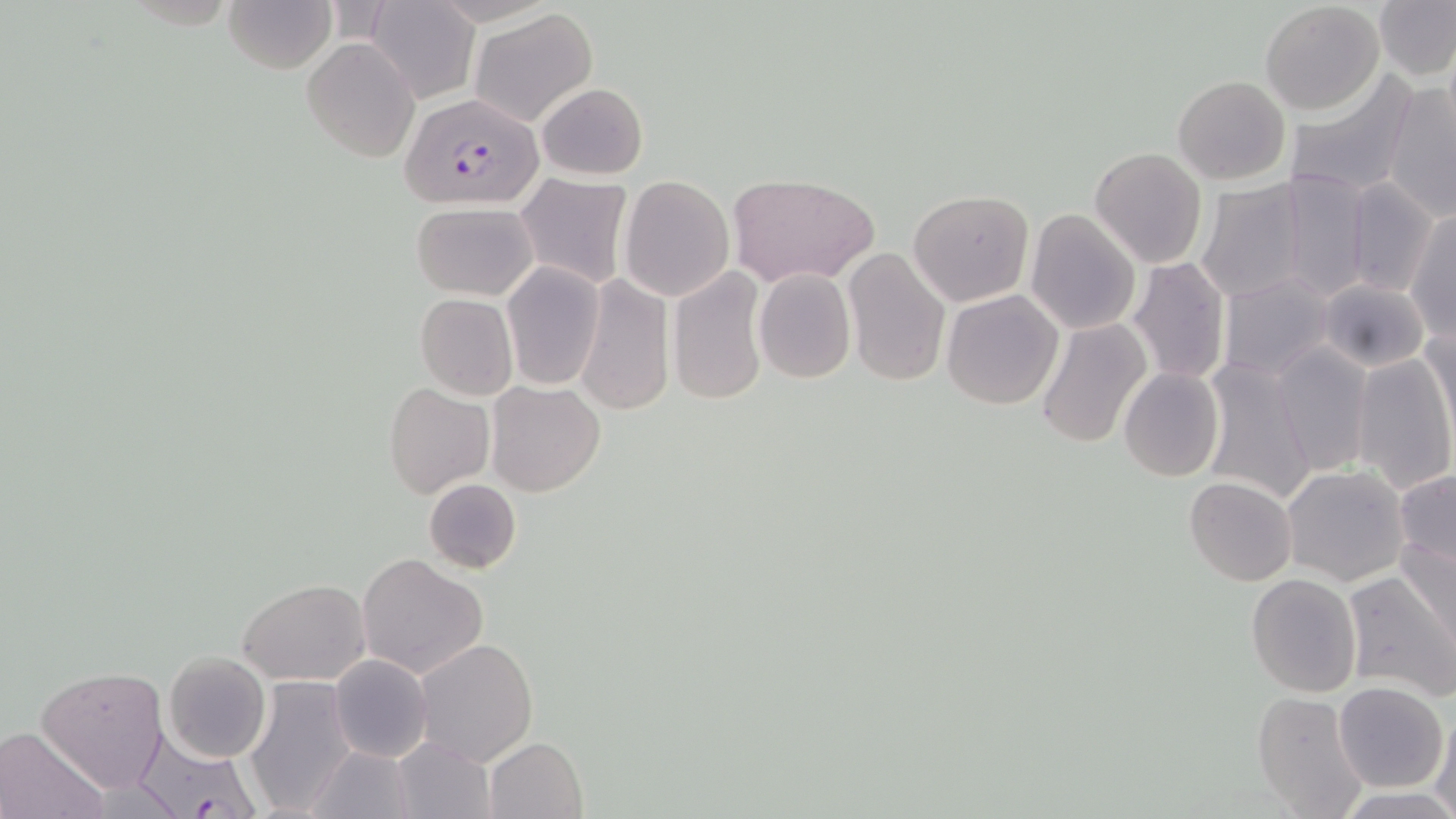
slide-level diagnosis = Plasmodium falciparum
field of view = single
modality = light microscopy
preparation = thin blood smear
uninfected red blood cell locations = approximate bounding boxes as (x1,y1)-(x2,y2) corner pairs in pixels: (223,0)-(336,73), (1375,0)-(1456,82), (369,1)-(479,104), (1260,3)-(1384,116), (471,9)-(598,126), (301,38)-(420,163), (1280,69)-(1420,201), (1172,74)-(1290,184), (537,82)-(649,180), (1383,82)-(1456,221), (1089,146)-(1207,269), (1273,173)-(1371,303), (727,174)-(878,287), (516,176)-(632,289), (619,176)-(735,301), (1195,180)-(1309,303), (1343,182)-(1438,298), (906,188)-(1035,307), (921,200)-(1051,397), (411,201)-(538,301), (1026,209)-(1141,334), (1407,210)-(1455,338), (843,249)-(950,386), (1125,257)-(1230,386), (501,262)-(605,390), (668,266)-(768,406), (754,268)-(856,383), (1218,272)-(1338,382), (576,273)-(674,417), (1318,278)-(1431,371), (940,289)-(1065,410), (414,292)-(519,400), (1036,317)-(1151,448), (1421,320)-(1455,438), (1269,344)-(1373,476), (1349,352)-(1455,497), (1199,358)-(1318,506), (1118,368)-(1224,481), (485,381)-(606,498), (385,382)-(495,499), (1282,465)-(1410,587), (1395,470)-(1456,573), (1184,477)-(1298,587), (424,478)-(523,575), (1398,537)-(1456,648), (356,553)-(488,679), (1340,570)-(1456,703), (1246,574)-(1362,696), (237,578)-(370,685), (415,638)-(539,766), (162,651)-(272,763), (329,654)-(434,763), (36,666)-(168,792), (243,677)-(356,816), (1334,683)-(1449,793), (1250,690)-(1370,819), (1430,708)-(1456,817), (1,726)-(107,819), (389,735)-(496,819), (484,737)-(587,819), (307,746)-(417,819), (1338,788)-(1453,818)
magnification = 1000x
stain = May-Grünwald-Giemsa
image size = 1456×819 pixels
Plasmodium falciparum-infected red blood cell locations = approximate bounding boxes as (x1,y1)-(x2,y2) corner pairs in pixels: (399,90)-(544,209), (139,736)-(264,819)